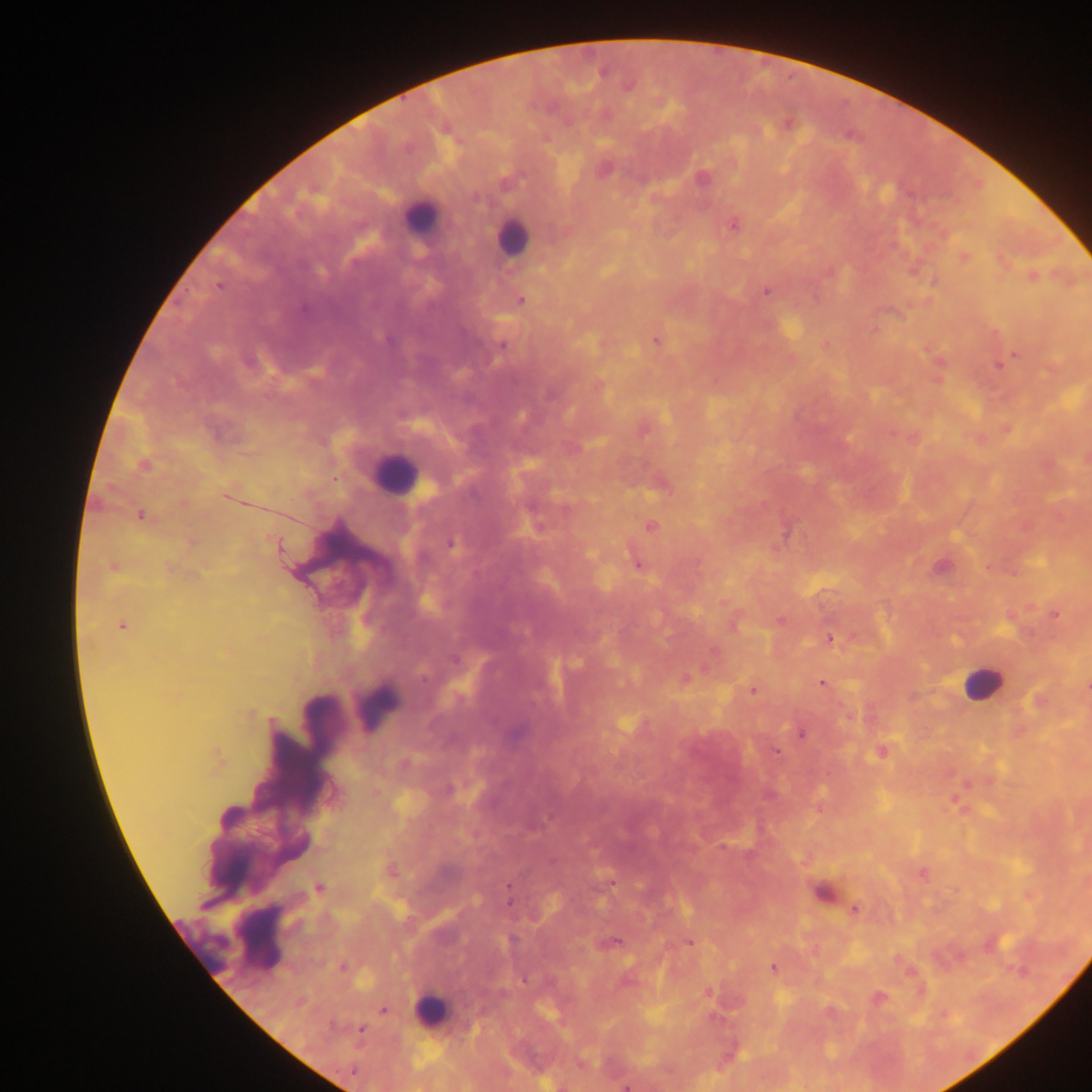

Approximate centers as (x, y) in pixels. Leukocyte locations: (417, 217), (511, 236), (394, 473), (982, 684), (378, 705), (260, 937), (200, 944), (432, 1008). Plasmodium parasite locations: (602, 72), (702, 179), (734, 225), (965, 257), (1033, 277), (218, 286), (766, 291), (521, 300), (304, 310), (656, 341), (503, 345), (1014, 355), (249, 362), (1002, 362), (550, 394), (142, 465), (141, 515), (651, 527), (451, 544), (278, 546), (638, 565), (113, 566), (941, 567), (1056, 614), (779, 620), (122, 626), (734, 626), (830, 638), (455, 659), (685, 678), (822, 683), (753, 690), (801, 734), (777, 752), (881, 752), (406, 764), (722, 847), (923, 875), (319, 889), (507, 889), (509, 901), (855, 909), (513, 940), (616, 941), (689, 942), (342, 967), (773, 969), (1018, 971), (524, 979), (880, 997), (383, 1010), (361, 1030), (626, 1086). Thick blood film. Collected in Ghana. Mobile-phone photograph taken through the microscope. One field of view. Image is 1092×1092 pixels.